Locate every Plasmodium parasite.
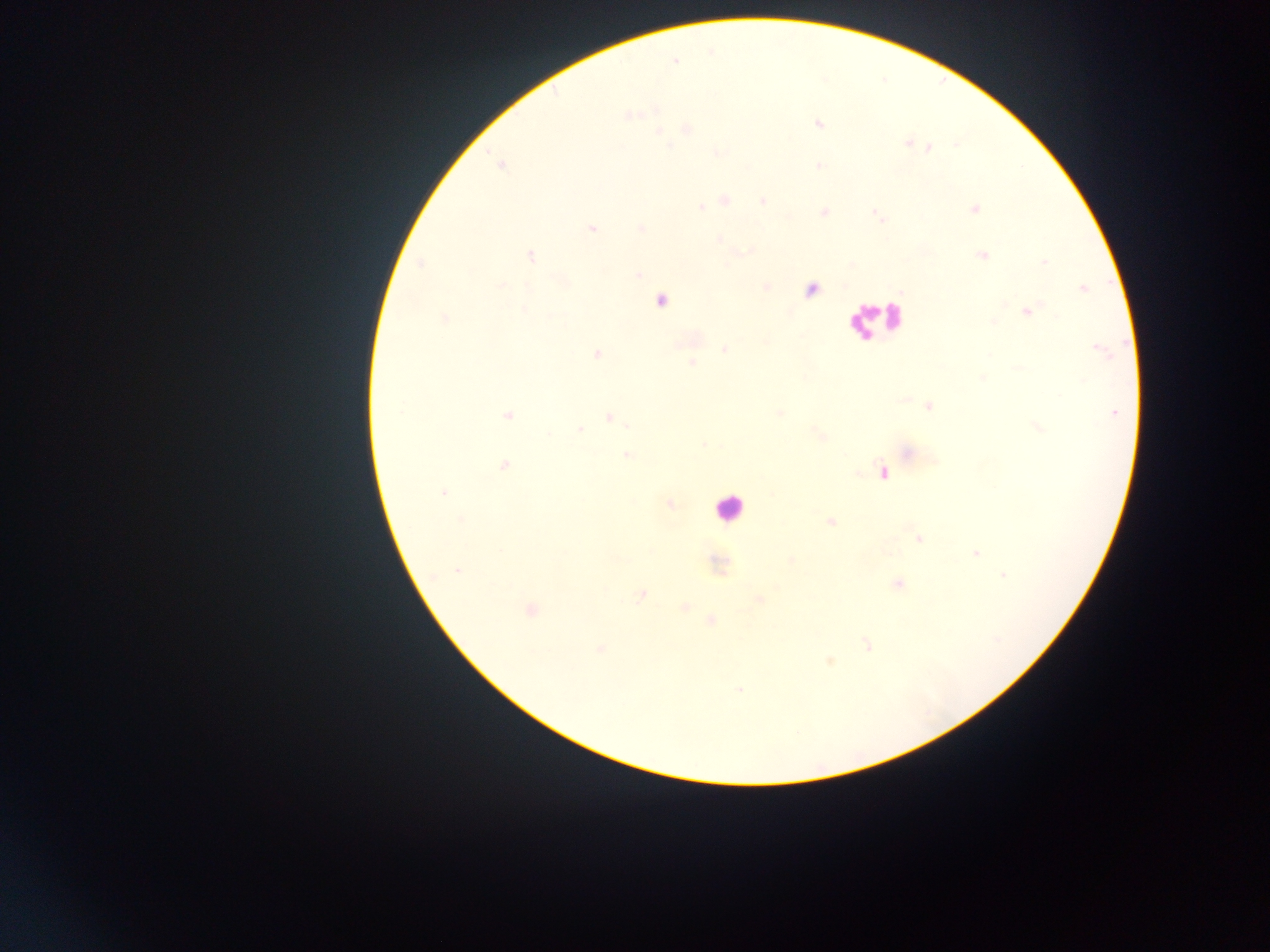
Approximate centers as x y in pixels.
Plasmodium parasites: 674 61; 630 115; 817 123; 685 127; 660 131; 906 142; 929 148; 819 165; 724 200; 763 201; 702 206; 974 209; 824 212; 592 228; 640 228; 719 239; 745 251; 531 256; 981 257; 1043 261; 418 263; 637 273; 501 285; 766 287; 1085 289; 662 300; 1030 311; 444 319; 687 339; 765 341; 725 349; 1101 350; 596 354; 692 362; 1017 369; 981 377; 927 405; 780 413; 1116 413; 508 416; 609 417; 1037 426; 579 430; 818 434; 704 444; 906 452; 626 455; 504 466; 883 471; 444 493; 671 504; 460 520; 831 521; 918 537; 501 550; 977 553; 616 558; 790 560; 457 570; 1004 575; 896 584; 641 596; 758 599; 685 606; 530 610; 711 620; 869 643; 600 648; 831 661; 740 690.

Summary:
  - Country: Ghana
  - Field of view: single
  - Capture: mobile-phone photograph through a microscope
  - Preparation: thick blood smear
  - Image size: 1270×952 pixels